Locate every uninfected red blood cell.
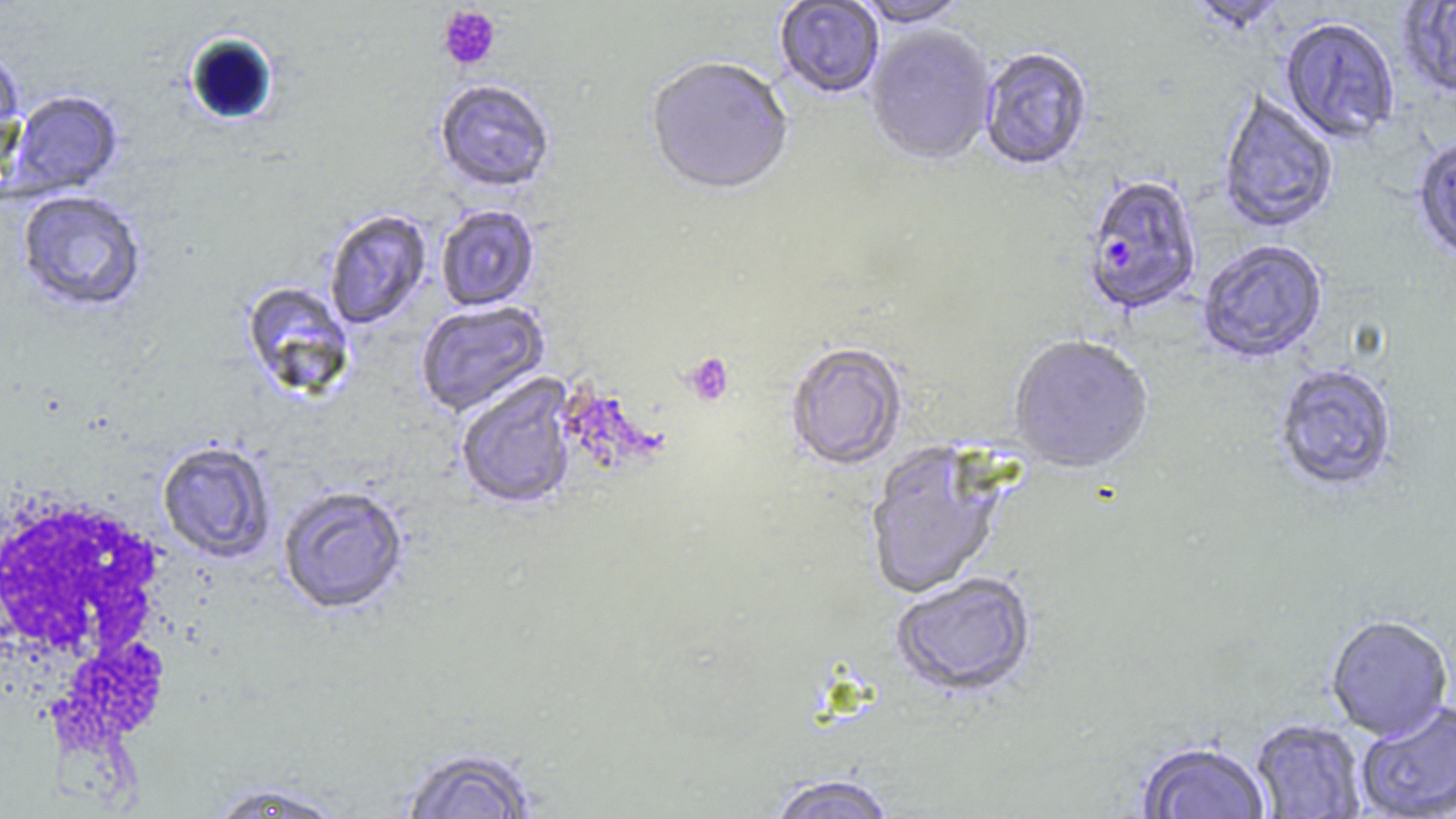
Approximate bounding boxes as (x1,y1)-(x2,y2) corner pairs in pixels.
Uninfected red blood cells: (774,0)-(885,100), (851,0)-(972,31), (1188,0)-(1288,35), (1399,1)-(1456,99), (1280,19)-(1399,145), (864,27)-(997,168), (0,47)-(25,172), (979,49)-(1093,173), (645,59)-(794,199), (434,80)-(556,194), (5,90)-(124,199), (1218,91)-(1338,235), (1413,138)-(1456,265), (16,189)-(148,314), (435,205)-(540,311), (323,209)-(432,330), (1198,241)-(1328,364), (240,282)-(356,401), (415,302)-(549,416), (1008,338)-(1153,476), (786,344)-(907,473), (1275,366)-(1399,493), (455,375)-(579,512), (157,440)-(276,564), (865,442)-(1006,601), (277,485)-(410,616), (892,575)-(1037,700), (1325,617)-(1453,743), (1356,703)-(1456,819), (1250,720)-(1367,818), (1135,743)-(1270,819), (399,746)-(540,818), (766,775)-(898,819), (204,781)-(349,818).

White blood cell locations: (2,488)-(186,793). Plasmodium falciparum-infected red blood cell locations: (1083,178)-(1201,317). Platelet locations: (437,4)-(502,72), (683,353)-(734,407). Slide-level diagnosis: Plasmodium falciparum. Light microscopy. Thin blood film. Image is 1456×819 pixels. One field of a larger specimen. Captured at 1000x magnification. May-Grünwald-Giemsa stain.